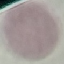

result: no malaria parasites detected
stain: Giemsa
preparation: thin blood smear
image_type: automatically extracted cell patch, resized to 64 × 64 pixels
capture: smartphone camera at the microscope eyepiece